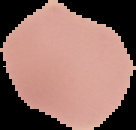 Image is 136×130 pixels. The area outside the segmented cell region is set to black. From a thin blood smear. Malaria status: uninfected.